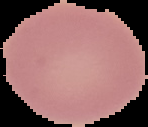 From a thin blood smear. Result: no malaria parasites seen. Segmented cell region on a black background. Image is 148×127 pixels.